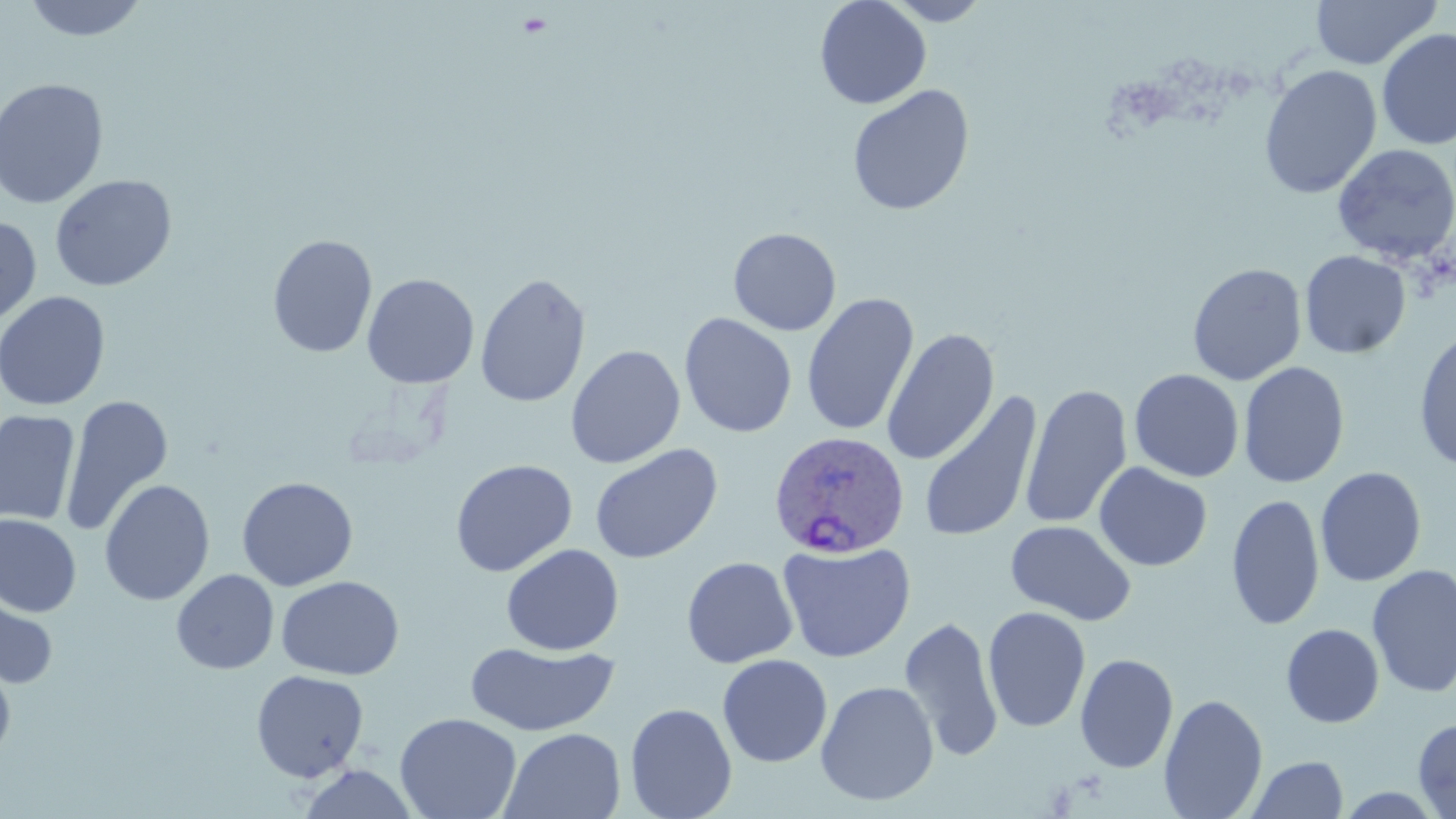

slide-level diagnosis = Plasmodium ovale
stain = May-Grünwald-Giemsa
magnification = 1000x
preparation = thin blood film
Plasmodium ovale-infected red blood cell locations = approximate bounding boxes as [x1, y1, x2, y2] in pixels: [768, 431, 910, 559]
image size = 1456×819 pixels
modality = optical microscopy
uninfected red blood cell locations = approximate bounding boxes as [x1, y1, x2, y2] in pixels: [22, 0, 150, 43], [814, 0, 931, 110], [881, 0, 993, 26], [1311, 0, 1442, 69], [1376, 28, 1455, 150], [1366, 29, 1456, 264], [1259, 64, 1382, 199], [0, 77, 109, 209], [847, 85, 975, 216], [1331, 143, 1456, 264], [50, 174, 177, 291], [0, 214, 41, 329], [728, 227, 841, 336], [267, 234, 378, 359], [1299, 250, 1411, 359], [1187, 263, 1307, 386], [474, 272, 591, 409], [362, 273, 480, 389], [0, 291, 111, 411], [801, 292, 919, 436], [678, 312, 798, 438], [882, 327, 999, 465], [1413, 329, 1456, 471], [566, 344, 685, 469], [1238, 361, 1350, 489], [1129, 369, 1244, 482], [1019, 383, 1133, 530], [919, 390, 1042, 543], [60, 395, 173, 538], [0, 410, 80, 527], [589, 443, 723, 564], [450, 459, 577, 577], [1094, 462, 1212, 572], [1315, 466, 1426, 587], [236, 476, 358, 591], [99, 479, 215, 606], [1226, 493, 1324, 631], [0, 514, 82, 618], [1006, 520, 1136, 626], [777, 540, 915, 663], [500, 543, 624, 656], [681, 556, 798, 668], [1366, 563, 1456, 698], [171, 569, 279, 674], [276, 575, 405, 680], [0, 581, 59, 691], [983, 606, 1090, 733], [899, 614, 1005, 761], [1281, 624, 1385, 728], [464, 642, 620, 736], [1075, 653, 1179, 773], [717, 654, 833, 767], [0, 656, 17, 765], [250, 669, 369, 782], [816, 680, 939, 806], [1159, 694, 1268, 819], [624, 702, 737, 819], [394, 712, 521, 819], [1413, 717, 1456, 818], [500, 727, 626, 818], [1245, 755, 1348, 818], [296, 764, 421, 819]
field of view = single